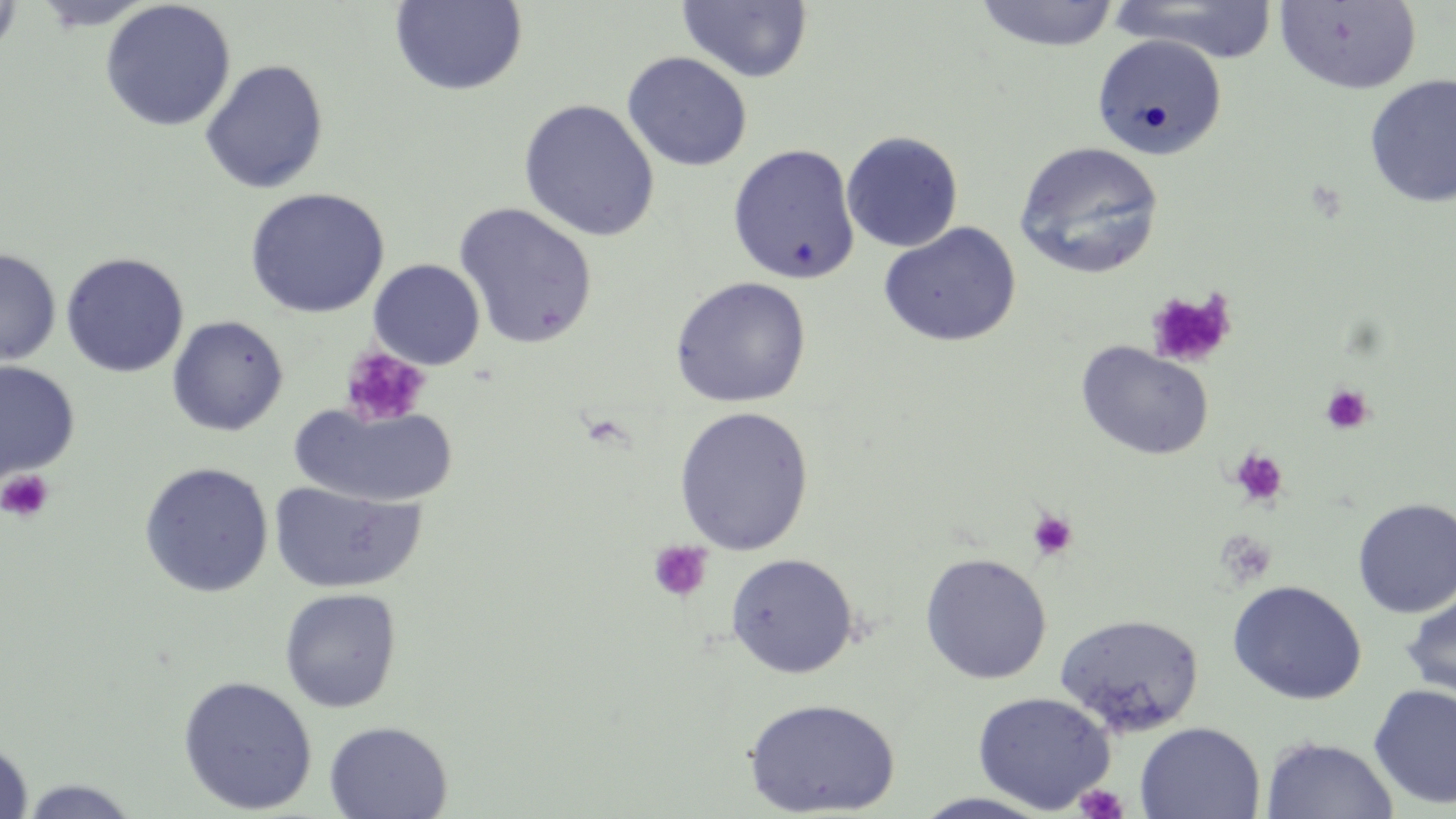
Summary:
  - Coordinate format: approximate bounding boxes as (x1, y1, x2, y2) in pixels
  - Uninfected red blood cell locations: (0, 0, 23, 62), (31, 0, 155, 31), (973, 0, 1120, 51), (1108, 0, 1280, 64), (99, 1, 236, 132), (389, 1, 528, 96), (677, 1, 813, 83), (1274, 1, 1423, 95), (1091, 33, 1227, 160), (622, 51, 753, 171), (200, 60, 329, 194), (1363, 73, 1456, 208), (518, 98, 660, 242), (841, 131, 964, 253), (1014, 142, 1164, 279), (727, 143, 861, 285), (244, 187, 390, 318), (453, 202, 599, 350), (878, 221, 1021, 347), (0, 248, 61, 368), (61, 252, 189, 377), (368, 259, 485, 370), (670, 276, 812, 408), (167, 315, 289, 436), (1076, 341, 1214, 461), (0, 361, 79, 482), (290, 402, 459, 509), (673, 406, 814, 555), (138, 462, 274, 597), (268, 480, 425, 594), (1351, 497, 1456, 617), (919, 552, 1052, 684), (726, 553, 859, 678), (1227, 580, 1367, 704), (1400, 587, 1456, 706), (279, 588, 401, 713), (1053, 611, 1207, 737), (178, 675, 317, 815), (1368, 682, 1456, 809), (972, 691, 1115, 813), (743, 697, 901, 818), (324, 721, 453, 818), (1134, 722, 1265, 819), (1260, 735, 1399, 819), (0, 738, 34, 819), (15, 778, 143, 818), (911, 792, 1057, 818)
  - Platelet locations: (1145, 287, 1238, 368), (339, 344, 431, 428), (1320, 383, 1374, 436), (1230, 449, 1288, 507), (0, 470, 54, 523), (1027, 509, 1078, 560), (1214, 529, 1278, 589), (648, 540, 713, 602), (1073, 784, 1129, 819)
  - Slide-level diagnosis: no evidence of blood parasites
  - Modality: light microscopy
  - Image size: 1456×819 pixels
  - Stain: May-Grünwald-Giemsa
  - Field of view: one of a larger specimen
  - Preparation: thin blood smear
  - Magnification: 1000x